Report the malaria status of this cell.
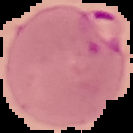

It is parasitized.

Summary:
  - Image size: 133×133 pixels
  - Image type: segmented cell region on a black background
  - Preparation: thin blood smear